Name the cell type shown.
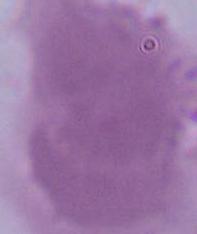
This is an erythrocyte.

modality = photomicrograph
magnification = 1000x